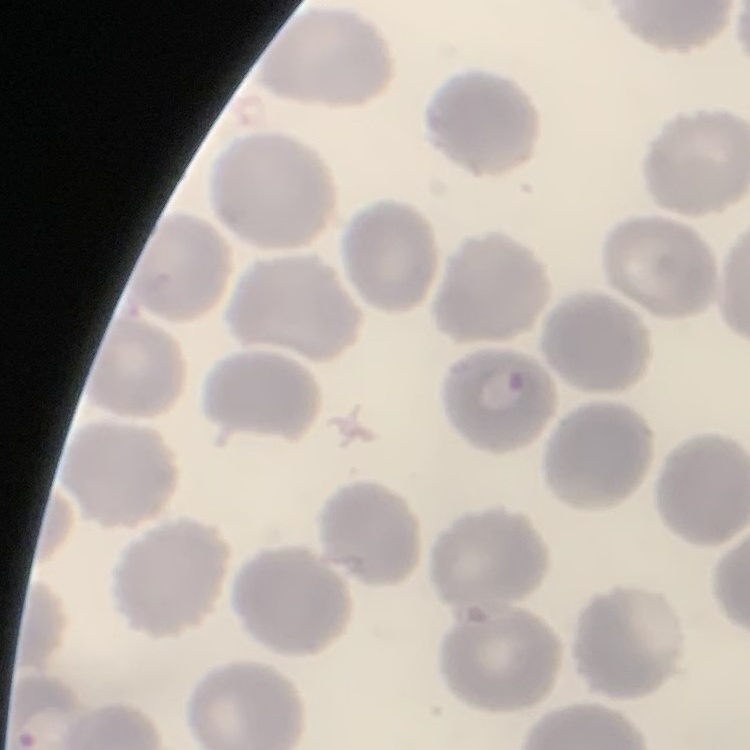

The red blood cells exhibit no rouleaux formation. Field's or Giemsa stain. Thin peripheral smear. Square crop of a larger photomicrograph.